Classify this cell by malaria status.
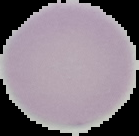
Uninfected.

Segmented cell region on a black background. Image is 139×136 pixels. From a thin blood film.